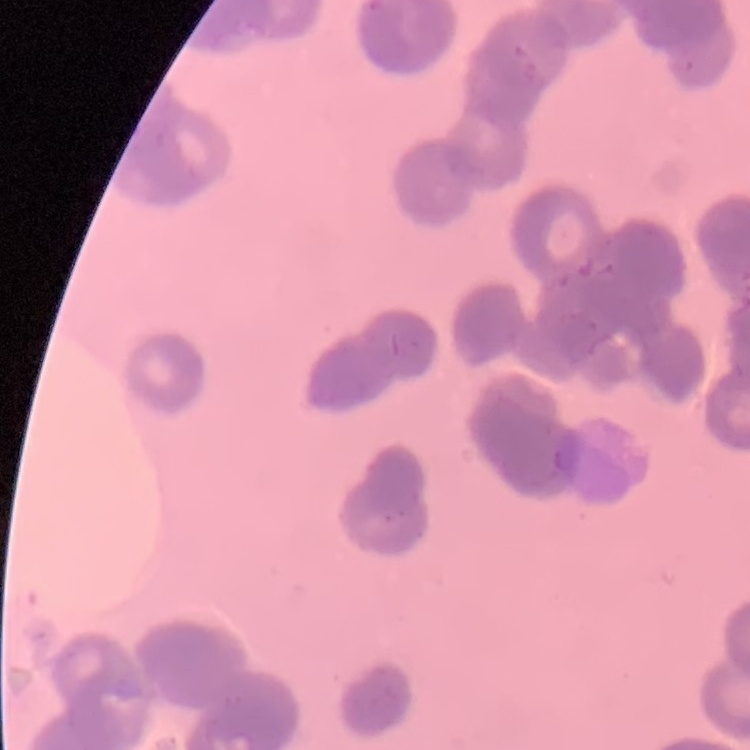
Summary:
  - Erythrocyte morphology: rouleaux formation
  - Preparation: thin blood film
  - Image type: one tile cut from a larger photomicrograph
  - Stain: Field's or Giemsa